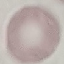
result = negative for malaria parasites
capture = smartphone camera at the microscope eyepiece
image type = automatically extracted cell patch, resized to 64 × 64 pixels
stain = Giemsa
preparation = thin smear